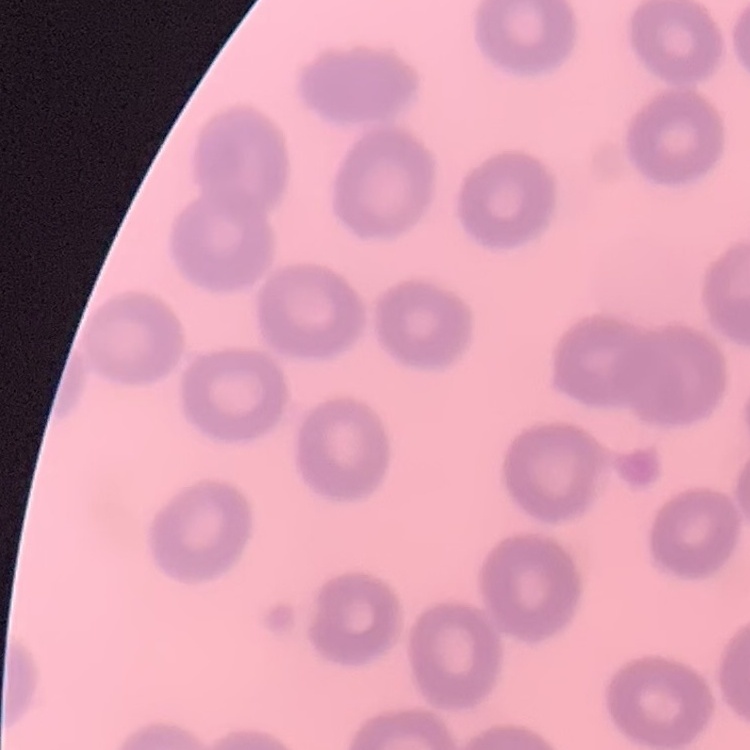 The erythrocytes exhibit no rouleaux formation. Square crop of a larger photomicrograph. Stained with either Field's or Giemsa. Thin blood smear.